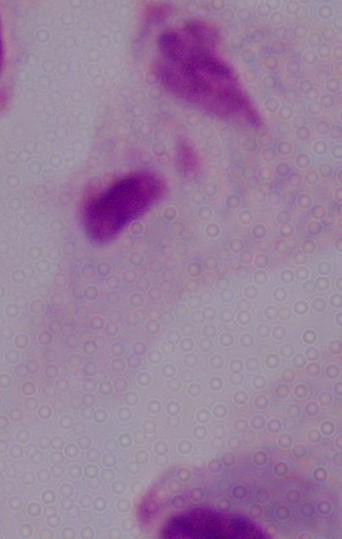
Micrograph. 1000x magnification. A trichomonad is seen.